Locate every blood parasite and identify its species.
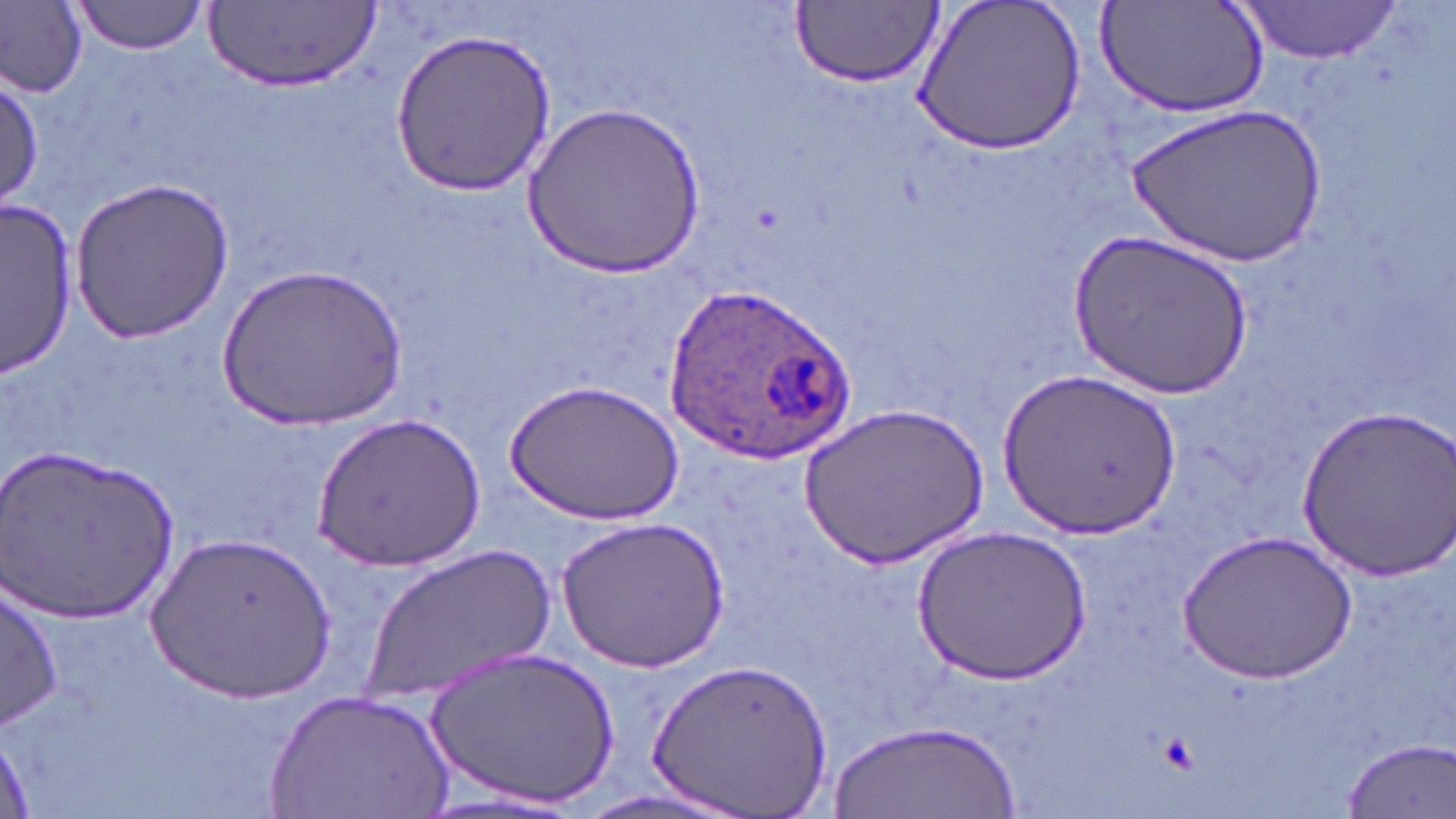
Approximate bounding boxes as (x1,y1)-(x2,y2) corner pairs in pixels.
Plasmodium ovale-infected red blood cells: (656,280)-(856,462).
No Plasmodium falciparum, Plasmodium malariae, Plasmodium vivax, Babesia divergens, or Trypanosoma brucei observed.

Uninfected red blood cell locations: (69,0)-(210,54), (914,0)-(1086,155), (1095,0)-(1269,120), (1233,0)-(1406,63), (789,1)-(941,87), (2,3)-(88,97), (210,3)-(377,94), (388,26)-(561,196), (1,74)-(44,210), (1132,100)-(1323,268), (524,102)-(706,276), (72,175)-(235,342), (1,200)-(79,378), (1069,229)-(1252,401), (219,265)-(405,430), (997,366)-(1179,538), (506,380)-(683,527), (801,403)-(987,568), (1292,403)-(1456,582), (312,411)-(480,571), (5,448)-(181,624), (558,516)-(730,672), (912,526)-(1091,684), (150,530)-(338,703), (1180,530)-(1354,684), (364,540)-(556,707), (2,578)-(64,733), (428,644)-(621,811), (647,655)-(835,817), (266,688)-(454,819), (831,721)-(1017,817), (0,736)-(35,815), (1339,737)-(1455,817), (433,789)-(593,817). Slide-level diagnosis: Plasmodium ovale. Image is 1456×819 pixels. Optical microscopy. 1000x magnification. One field of a larger specimen. Thin blood smear. May-Grünwald-Giemsa-stained preparation.